Assess this cell for malaria.
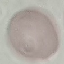

Uninfected.

preparation = thin blood smear
image type = cell patch, automatically extracted from a larger field of view and resized to 64 × 64 pixels
stain = Giemsa
capture = smartphone camera at the microscope eyepiece